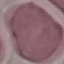 Result: no malaria parasites seen. Photographed with a smartphone camera at the microscope eyepiece. Giemsa-stained preparation. Thin blood film. Cell patch, automatically extracted from a larger field of view and resized to 64 × 64 pixels.